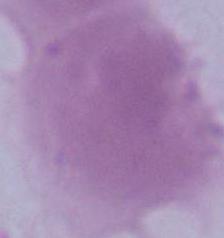

A red blood cell is shown. Photomicrograph. 1000x magnification.